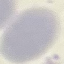
result = no malaria parasites seen
capture = smartphone camera at the microscope eyepiece
stain = Giemsa
image type = automatically extracted cell patch, resized to 64 × 64 pixels
preparation = thin smear